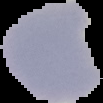
Segmented cell region on a black background. Image is 103×103 pixels. From a thin blood smear. Malaria status: uninfected.